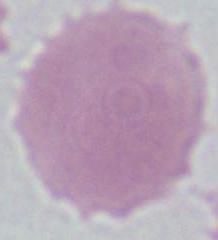

{
  "identification": "red blood cell",
  "magnification": "1000x",
  "modality": "photomicrograph"
}